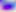 Captured at 400x magnification. Micrograph. Toxoplasma gondii is shown.